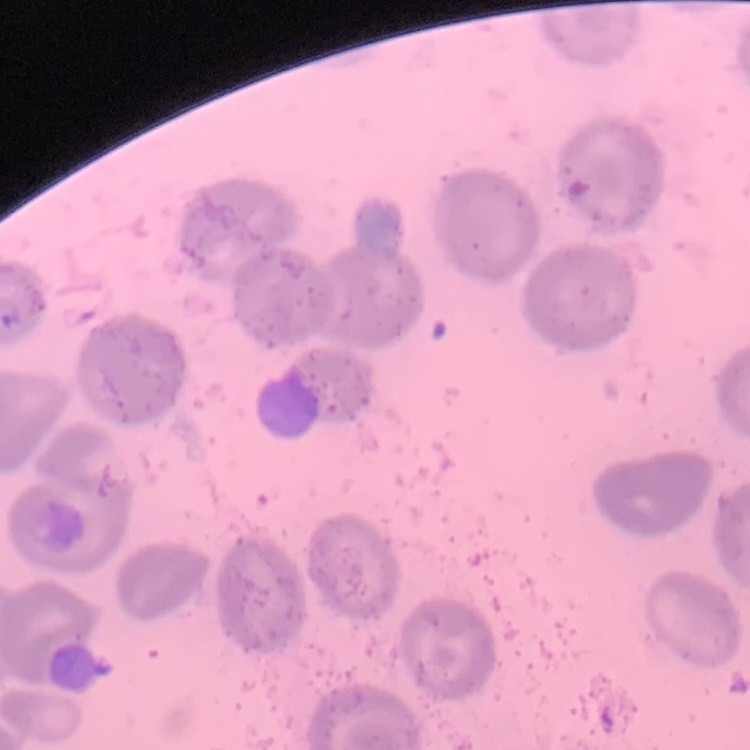

Summary:
  - Red blood cell morphology: no rouleaux formation
  - Preparation: thin peripheral smear
  - Image type: one tile cut from a larger photomicrograph
  - Stain: Field's or Giemsa